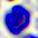 A leukocyte is seen. Micrograph. 400x magnification.